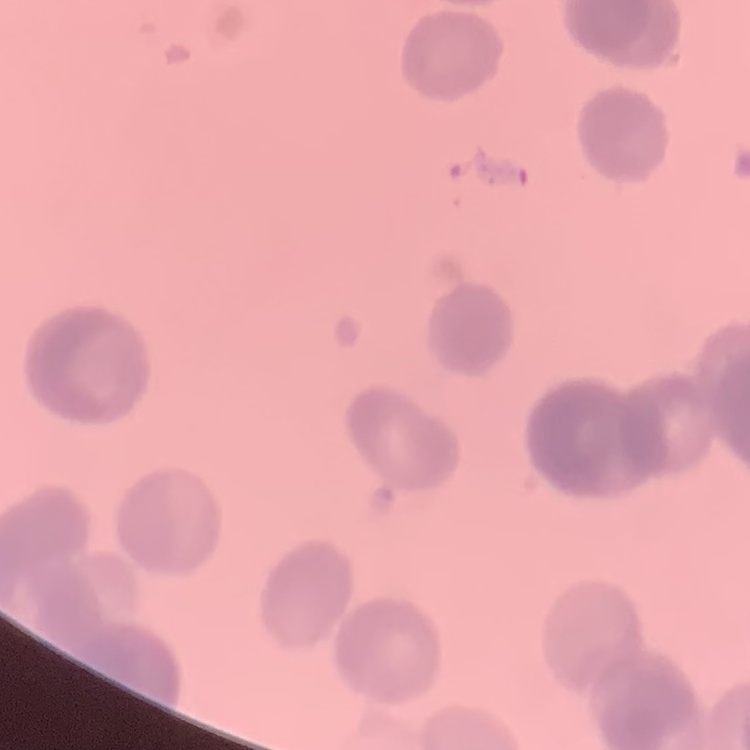 The erythrocytes show rouleaux formation. Field's or Giemsa stain. Thin blood smear. One tile cut from a larger photomicrograph.